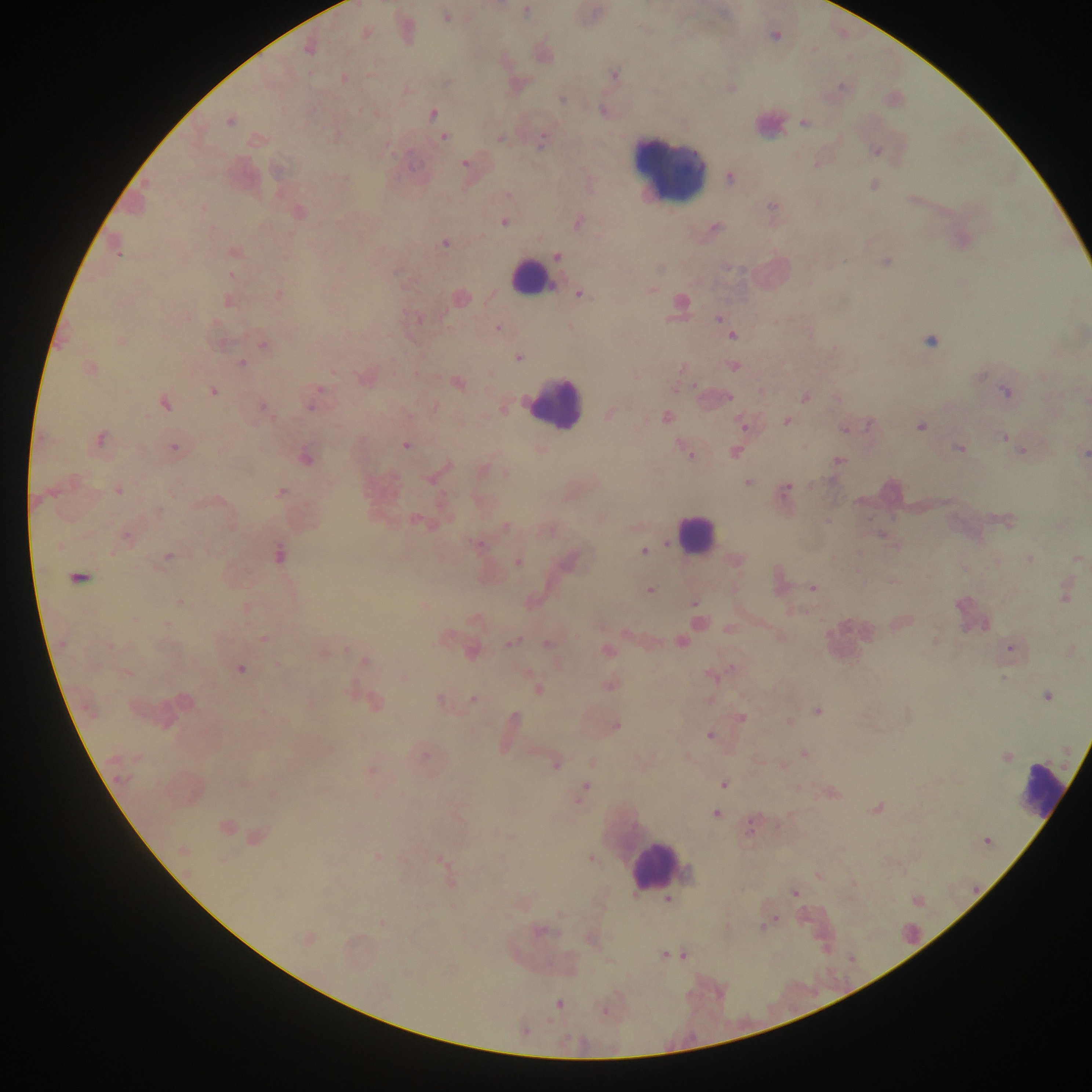

field of view = single
capture = mobile-phone photograph through a microscope
leukocyte locations = approximate centers as (x, y) in pixels: (671, 165), (527, 277), (554, 404), (696, 533), (1043, 788), (654, 865)
preparation = thick blood smear
image size = 1092×1092 pixels
country = Ghana
malaria parasite locations = approximate centers as (x, y) in pixels: (526, 10), (446, 18), (366, 33), (775, 36), (309, 49), (614, 74), (343, 78), (562, 99), (433, 113), (229, 121), (803, 123), (443, 137), (500, 138), (542, 139), (464, 164), (730, 177), (873, 185), (771, 206), (203, 208), (299, 212), (504, 222), (578, 222), (714, 228), (444, 244), (116, 248), (234, 251), (557, 255), (887, 262), (231, 276), (650, 290), (279, 295), (579, 295), (460, 297), (229, 301), (681, 301), (418, 319), (719, 320), (497, 328), (732, 336), (122, 341), (931, 341), (263, 345), (518, 357), (240, 363), (734, 366), (89, 369), (458, 383), (319, 389), (212, 391), (1006, 392), (729, 397), (805, 397), (1086, 401), (165, 404), (311, 407), (264, 408), (434, 408), (609, 414), (667, 417), (786, 421), (868, 425), (743, 426), (921, 426), (846, 429), (1004, 437), (100, 439), (406, 445), (173, 448), (960, 449), (540, 450), (1021, 451), (1085, 452), (735, 453), (688, 454), (305, 457), (837, 461), (448, 466), (506, 473), (427, 478), (747, 483), (119, 491), (785, 491), (281, 492), (158, 512), (1008, 521), (420, 522), (506, 526), (127, 538), (475, 543), (58, 546), (645, 551), (279, 555), (168, 556), (1077, 558), (1029, 559), (738, 560), (518, 562), (78, 577), (812, 588), (649, 590), (1065, 597), (181, 602), (694, 603), (135, 619), (699, 621), (905, 622), (264, 639), (935, 641), (512, 642), (680, 642), (547, 644), (110, 646), (1011, 648), (346, 649), (607, 651), (472, 653), (366, 662), (241, 669), (126, 672), (711, 675), (1004, 678), (609, 684), (538, 688), (1046, 696), (473, 699), (440, 701), (376, 703), (817, 711), (741, 717), (514, 718), (616, 725), (709, 735), (804, 753), (1006, 757), (556, 764), (370, 771), (724, 784), (582, 791), (877, 808), (716, 814), (752, 825), (225, 827), (257, 836), (988, 841), (183, 850), (377, 857), (591, 859), (222, 861), (441, 862), (687, 871), (795, 893), (668, 899), (384, 924), (541, 931), (307, 938), (665, 955), (685, 956), (559, 1004)